Mark where leukocytes are.
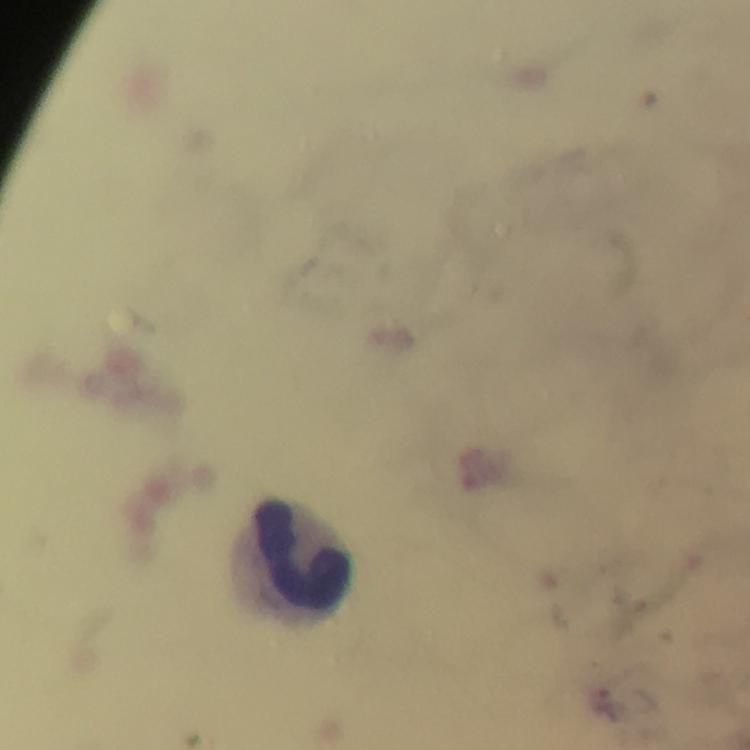

Approximate centers as (x, y) in pixels.
Leukocytes: (303, 555).

{
  "image_size": "750×750 pixels",
  "cropped_from": "a single field of view",
  "context": "from a malaria diagnostic workup",
  "capture": "smartphone camera through the microscope",
  "plasmodium_parasite_locations": "approximate centers as (x, y) in pixels: (606, 702)",
  "immersion_oil": "used",
  "stain": "Giemsa",
  "preparation": "thick blood smear",
  "magnification": "100x"
}